Give the position of every leukocyte visible.
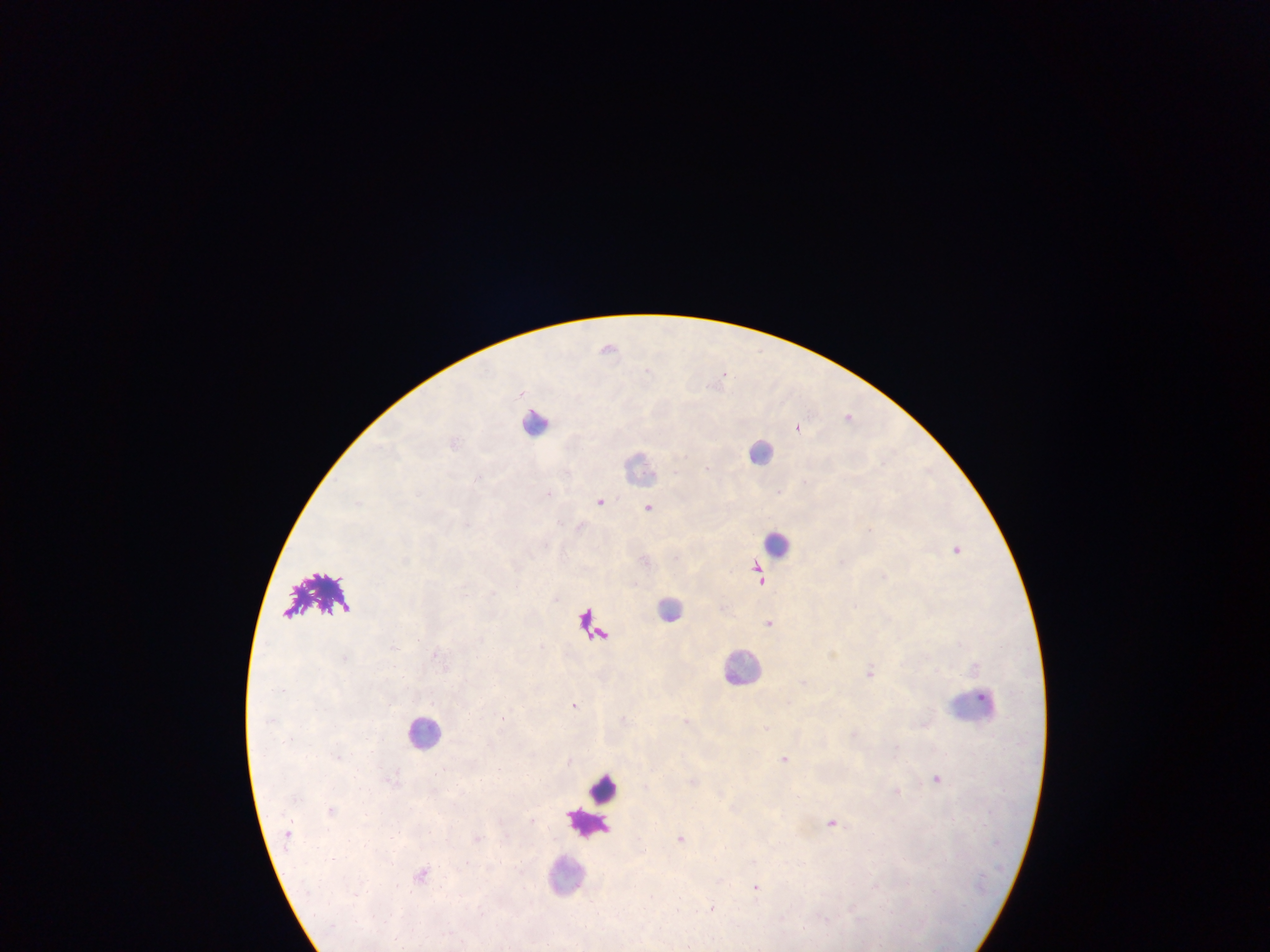

Approximate centers as (x, y) in pixels.
Leukocytes: (538, 421), (761, 451), (640, 467), (777, 544), (671, 608), (742, 666), (973, 703), (426, 731), (604, 790), (586, 822), (565, 875).

field of view = single
image size = 1270×952 pixels
country = Ghana
Plasmodium parasite locations = approximate centers as (x, y) in pixels: (608, 347), (724, 374), (849, 415), (798, 426), (708, 467), (475, 478), (549, 494), (600, 500), (359, 502), (649, 507), (580, 525), (957, 550), (884, 575), (759, 577), (769, 622), (346, 657), (870, 671), (574, 704), (502, 717), (784, 758), (937, 778), (833, 822), (681, 838), (422, 874), (756, 887), (713, 906), (678, 908)
capture = mobile-phone photograph through a microscope
preparation = thick blood smear